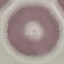
malaria status = uninfected
preparation = thin blood smear
capture = smartphone camera at the microscope eyepiece
image type = cell patch, automatically extracted from a larger field of view and resized to 64 × 64 pixels
stain = Giemsa